Outline each blood parasite and name the species.
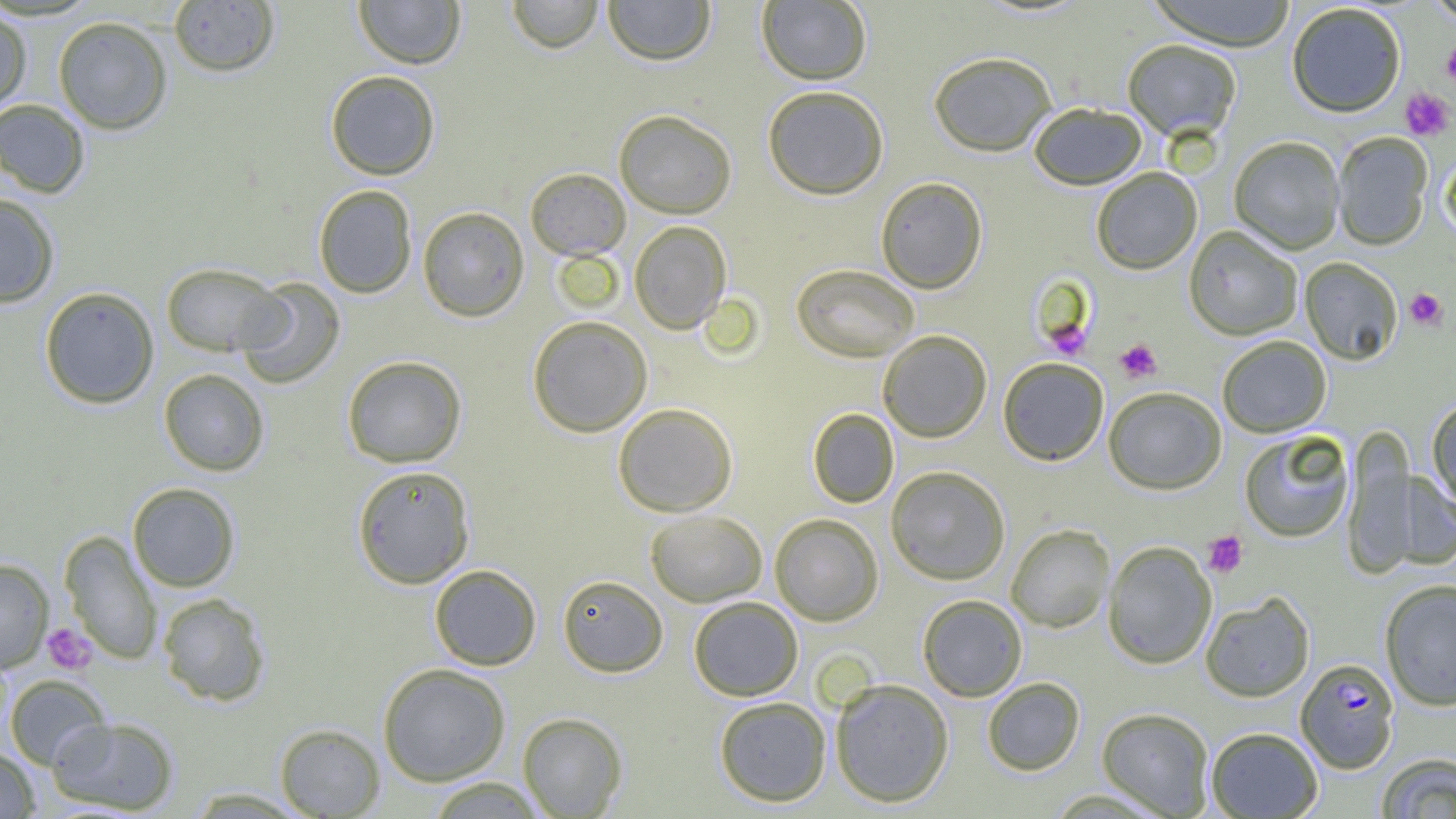
Approximate bounding boxes as (x1,y1)-(x2,y2) corner pairs in pixels.
Plasmodium falciparum-infected red blood cells: (1295,658)-(1399,773).
No Plasmodium ovale, Plasmodium malariae, Plasmodium vivax, Babesia divergens, or Trypanosoma brucei observed.

Summary:
  - Uninfected red blood cell locations: (353,0)-(465,69), (506,0)-(604,53), (602,0)-(716,66), (1146,0)-(1298,51), (1423,0)-(1456,25), (168,1)-(280,77), (757,1)-(872,85), (1286,4)-(1406,118), (0,7)-(32,113), (53,16)-(172,134), (1122,39)-(1241,141), (928,51)-(1057,157), (325,70)-(441,180), (762,85)-(889,200), (0,99)-(91,198), (1029,102)-(1147,190), (614,109)-(737,219), (1332,132)-(1433,251), (1229,137)-(1344,255), (1441,151)-(1456,245), (525,167)-(631,260), (1091,167)-(1203,275), (875,176)-(988,293), (313,185)-(417,298), (0,193)-(60,308), (417,206)-(530,321), (629,220)-(732,334), (1183,226)-(1302,341), (1299,257)-(1403,365), (161,262)-(287,357), (791,264)-(920,363), (234,278)-(346,389), (39,286)-(160,409), (527,316)-(652,437), (878,330)-(992,442), (1218,336)-(1331,437), (342,355)-(467,468), (998,358)-(1109,466), (158,369)-(270,476), (1103,387)-(1226,495), (1426,399)-(1456,515), (612,402)-(738,517), (808,408)-(898,508), (1343,428)-(1420,579), (1239,430)-(1354,543), (352,464)-(475,588), (886,466)-(1010,585), (1387,471)-(1456,570), (127,482)-(241,592), (645,510)-(767,607), (769,513)-(883,626), (1006,524)-(1114,633), (59,531)-(162,665), (1102,541)-(1216,670), (0,559)-(53,672), (429,564)-(542,671), (557,574)-(668,677), (1379,579)-(1456,711), (157,592)-(271,707), (1200,592)-(1315,703), (917,594)-(1027,701), (688,596)-(803,701), (377,663)-(511,786), (4,674)-(111,770), (830,678)-(954,807), (982,678)-(1085,775), (714,695)-(831,807), (1097,707)-(1214,817), (517,712)-(627,818), (48,716)-(179,814), (274,723)-(386,818), (1206,727)-(1322,818), (0,748)-(40,818), (1376,754)-(1456,818), (425,777)-(548,818), (183,787)-(313,817)
  - Platelet locations: (1442,40)-(1456,86), (1399,87)-(1454,141), (1405,288)-(1447,329), (1043,315)-(1093,361), (1115,339)-(1162,383), (1202,531)-(1248,578), (43,623)-(97,675)
  - Slide-level diagnosis: Plasmodium falciparum
  - Image size: 1456×819 pixels
  - Field of view: one of a larger specimen
  - Preparation: thin blood smear
  - Magnification: 1000x
  - Modality: light microscopy